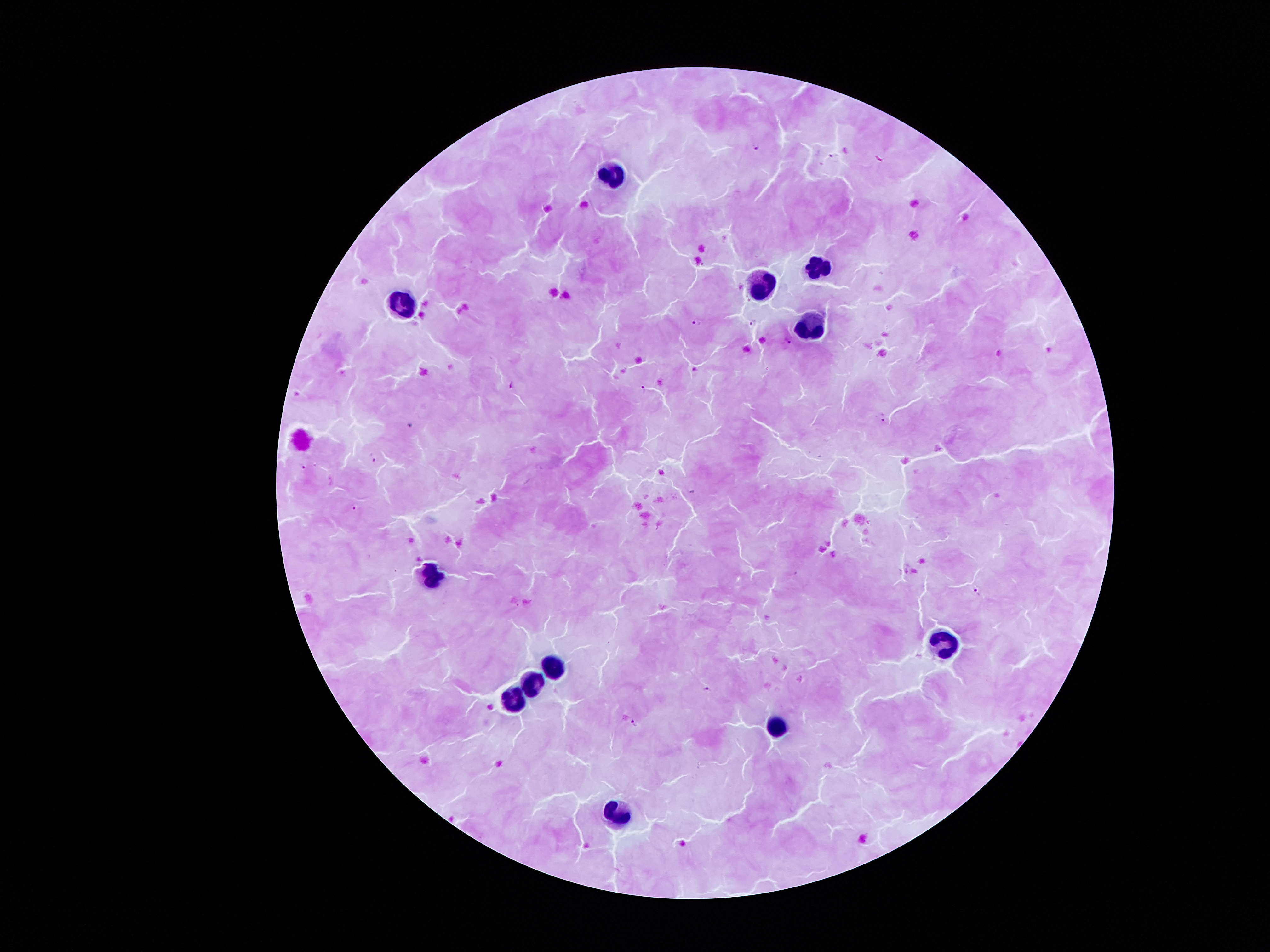

Approximate object centers, in pixels from the top-left corner. Plasmodium parasite locations: (x=757, y=147), (x=831, y=155), (x=695, y=321), (x=754, y=322), (x=788, y=340), (x=512, y=383), (x=643, y=389), (x=882, y=418), (x=411, y=422), (x=373, y=460), (x=305, y=467), (x=354, y=505), (x=977, y=590), (x=707, y=688), (x=632, y=723). Leukocyte locations: (x=611, y=172), (x=818, y=265), (x=763, y=283), (x=402, y=302), (x=811, y=326), (x=433, y=578), (x=948, y=641), (x=556, y=668), (x=538, y=683), (x=515, y=697), (x=773, y=725), (x=616, y=815). Smartphone photograph taken through the microscope eyepiece. 100x magnification. Image is 1270×952 pixels. Thick peripheral-blood smear. Giemsa stain. Patient malaria status: positive for Plasmodium falciparum. Single field of view.